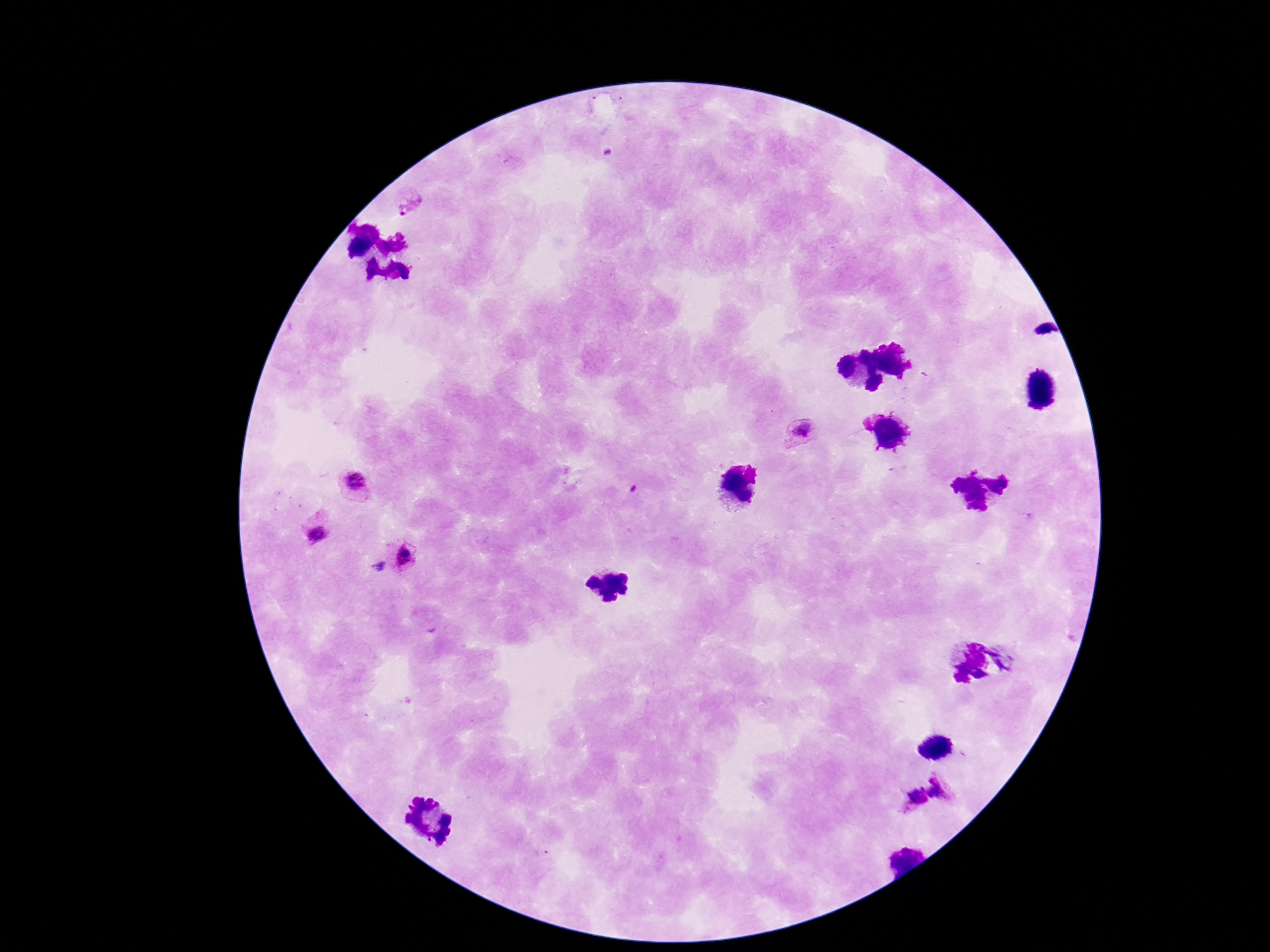

{
  "magnification": "100x",
  "image_size": "1270×952 pixels",
  "capture": "smartphone camera through the microscope eyepiece",
  "stain": "Giemsa",
  "preparation": "thick blood film",
  "patient_malaria_status": "infected",
  "field_of_view": "single",
  "plasmodium_parasite_locations": "approximate centers as {x, y} in pixels: {407, 199}, {801, 432}, {355, 484}, {316, 530}, {406, 557}, {944, 785}, {913, 797}"
}